Outline platelets.
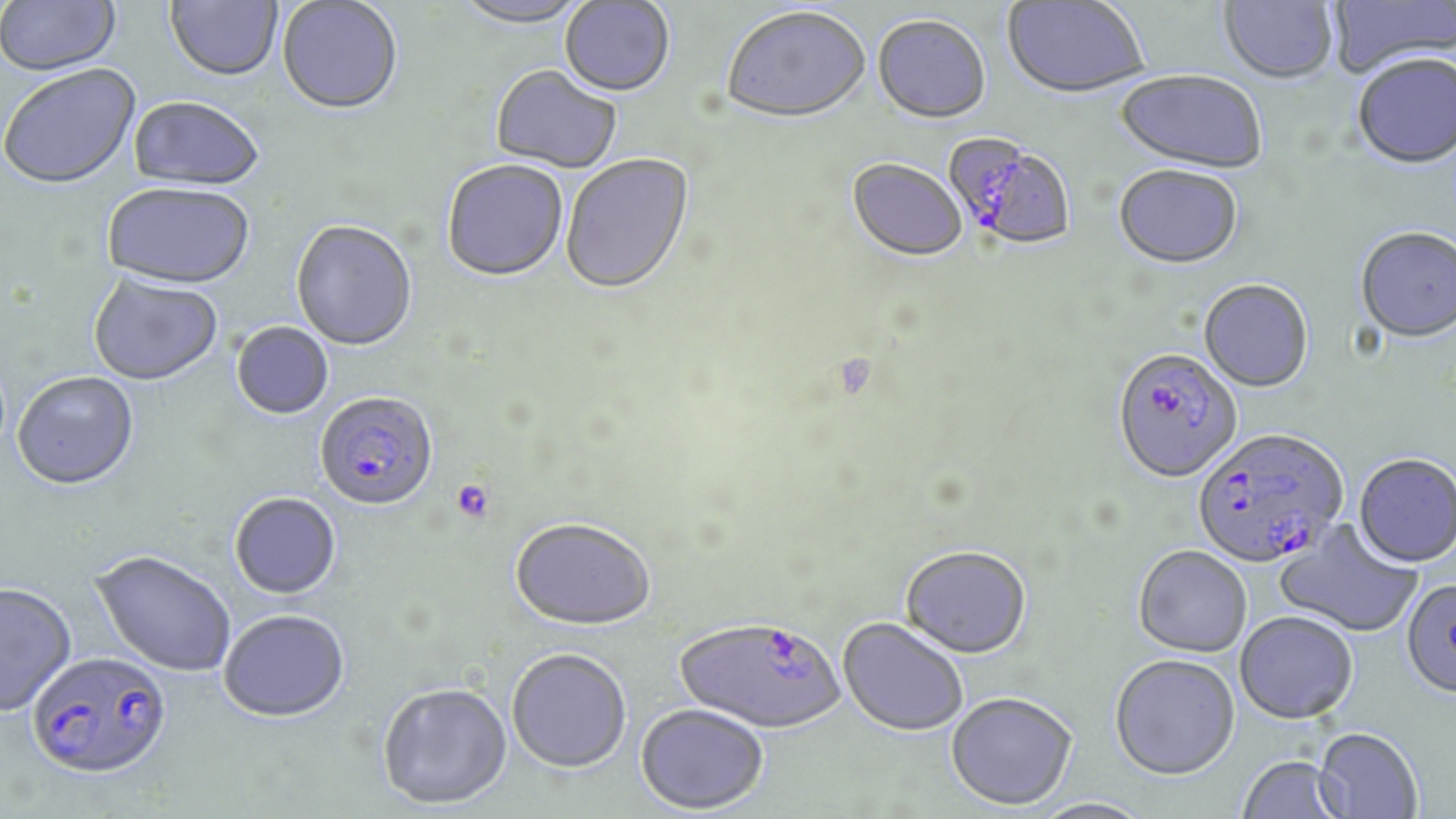

Approximate bounding boxes as (x1, y1, x2, y2) in pixels.
Platelets: (451, 479, 495, 523).

Summary:
  - Plasmodium falciparum-infected red blood cell locations: (944, 134, 1077, 254), (1112, 350, 1243, 485), (315, 393, 439, 514), (1192, 429, 1348, 572), (675, 619, 846, 736), (26, 652, 173, 783)
  - Uninfected red blood cell locations: (1, 0, 122, 78), (164, 0, 283, 84), (1003, 0, 1148, 100), (1218, 0, 1338, 87), (1327, 0, 1455, 80), (277, 1, 403, 117), (451, 1, 593, 31), (560, 1, 675, 100), (722, 9, 871, 126), (872, 17, 991, 126), (1353, 56, 1456, 172), (1, 66, 142, 193), (490, 66, 621, 176), (1115, 71, 1266, 176), (128, 98, 263, 193), (561, 155, 696, 298), (847, 160, 968, 264), (441, 161, 569, 284), (1113, 167, 1243, 272), (102, 186, 254, 293), (291, 222, 418, 353), (1355, 229, 1456, 346), (88, 274, 224, 388), (1199, 280, 1314, 394), (231, 322, 334, 421), (12, 373, 140, 493), (1353, 455, 1456, 570), (229, 494, 342, 601), (509, 520, 655, 634), (1274, 520, 1423, 639), (1133, 546, 1252, 658), (900, 547, 1032, 661), (89, 551, 235, 678), (1400, 579, 1456, 701), (0, 585, 77, 718), (219, 612, 351, 725), (1235, 612, 1358, 726), (838, 619, 969, 738), (507, 651, 631, 775), (1109, 655, 1241, 782), (377, 685, 513, 812), (945, 694, 1077, 812), (635, 706, 769, 816), (1314, 727, 1423, 818), (1235, 756, 1348, 819), (1031, 798, 1154, 819)
  - Slide-level diagnosis: Plasmodium falciparum
  - Modality: light microscopy
  - Field of view: single
  - Magnification: 1000x
  - Stain: May-Grünwald-Giemsa
  - Preparation: thin blood smear
  - Image size: 1456×819 pixels